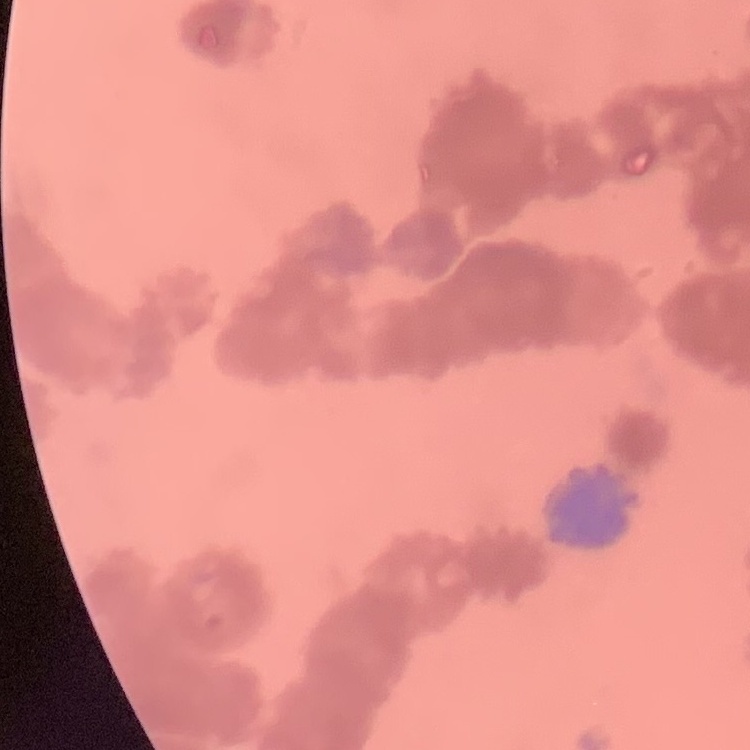
erythrocyte morphology = rouleaux formation
image type = square crop of a larger photomicrograph
preparation = thin peripheral smear
stain = Field's or Giemsa